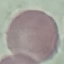

Malaria status: uninfected. Giemsa-stained preparation. Cell patch, automatically extracted from a larger field of view and resized to 64 × 64 pixels. Acquired by smartphone through the microscope eyepiece. Thin blood film.